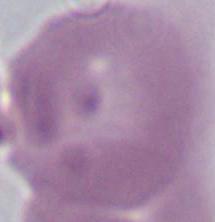

Summary:
  - Identification: red blood cell
  - Modality: photomicrograph
  - Magnification: 1000x